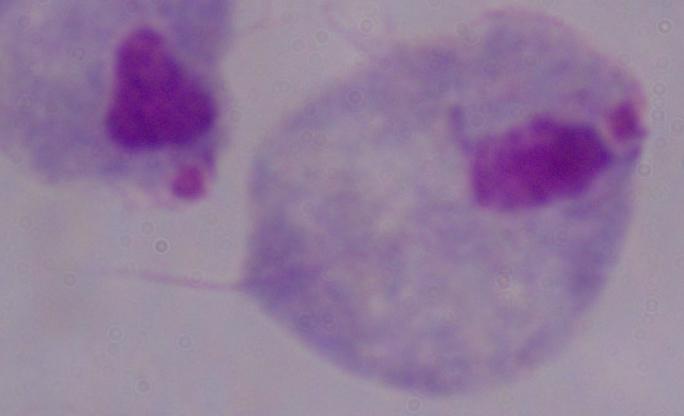
Summary:
  - Identification: trichomonad
  - Magnification: 1000x
  - Modality: micrograph